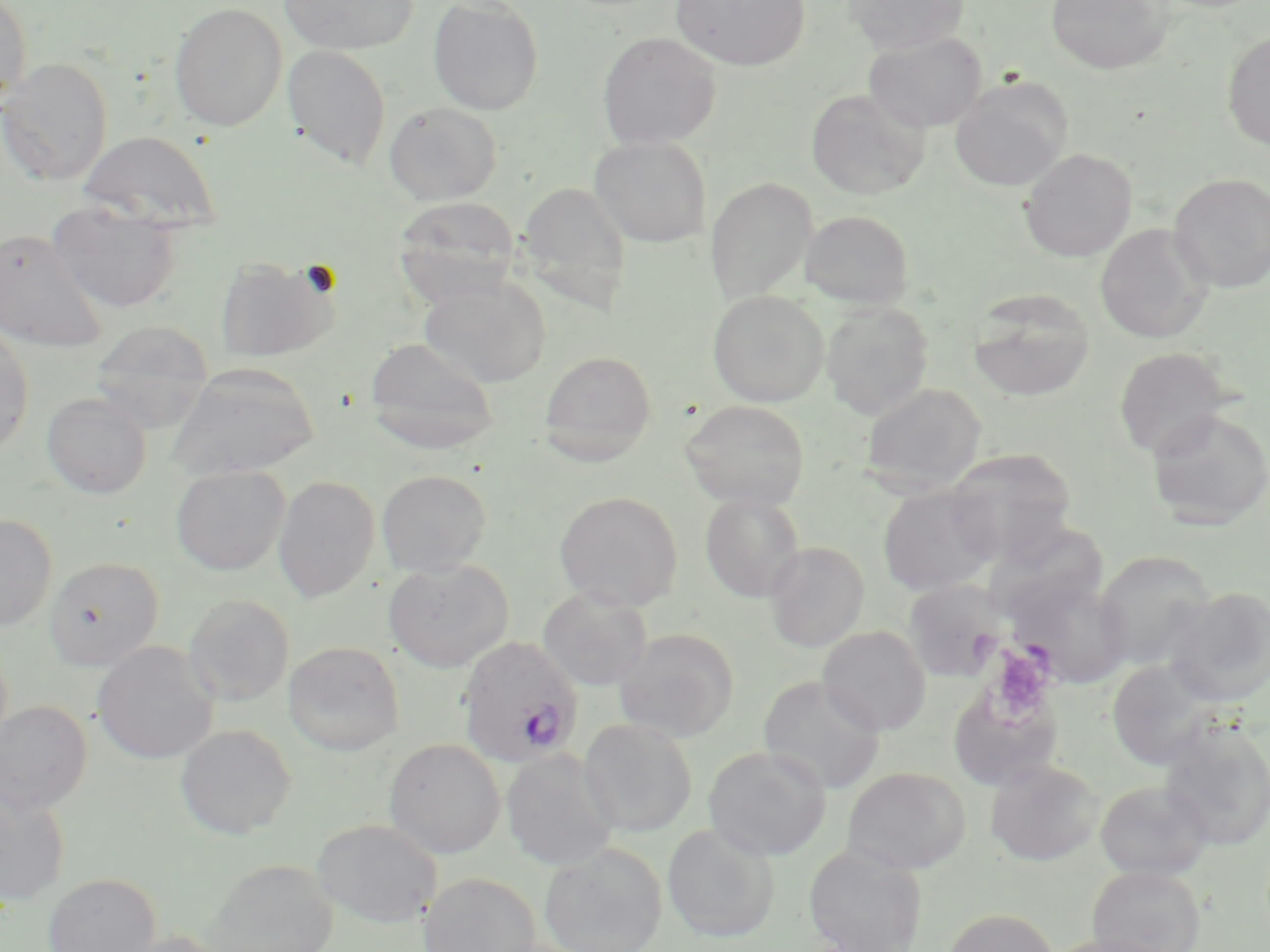 Approximate bounding boxes as (x1, y1, x2, y2) in pixels. Uninfected red blood cell locations: (0, 0, 32, 112), (278, 0, 417, 55), (427, 0, 544, 116), (670, 0, 810, 71), (842, 0, 968, 54), (1046, 0, 1174, 74), (169, 1, 288, 131), (1221, 30, 1270, 151), (597, 31, 722, 150), (863, 31, 987, 132), (281, 44, 392, 168), (0, 57, 113, 185), (949, 75, 1072, 192), (806, 88, 930, 200), (384, 101, 502, 205), (79, 130, 222, 232), (589, 136, 711, 247), (1019, 148, 1137, 261), (1168, 173, 1270, 293), (705, 177, 818, 304), (516, 181, 632, 310), (392, 196, 521, 305), (47, 202, 183, 314), (799, 210, 914, 309), (1095, 223, 1212, 343), (0, 228, 109, 354), (215, 255, 341, 362), (419, 277, 552, 387), (968, 287, 1095, 401), (707, 290, 829, 407), (821, 301, 934, 419), (89, 319, 215, 432), (0, 323, 35, 457), (364, 337, 500, 453), (1112, 347, 1233, 461), (538, 350, 657, 465), (167, 362, 320, 479), (859, 383, 987, 495), (42, 392, 151, 498), (680, 399, 811, 510), (1146, 408, 1270, 530), (944, 447, 1078, 563), (171, 465, 291, 575), (377, 469, 492, 576), (273, 475, 380, 602), (878, 485, 998, 596), (554, 490, 684, 611), (700, 492, 805, 602), (0, 514, 58, 631), (764, 542, 869, 652), (1094, 550, 1216, 670), (44, 557, 164, 669), (383, 559, 514, 671), (1006, 573, 1133, 688), (903, 579, 1008, 682), (537, 587, 653, 691), (1164, 587, 1270, 706), (183, 594, 294, 707), (818, 625, 931, 735), (614, 627, 740, 742), (283, 640, 405, 755), (93, 641, 219, 764), (1107, 660, 1218, 770), (757, 675, 886, 794), (947, 685, 1062, 792), (0, 700, 93, 815), (578, 718, 698, 836), (1158, 720, 1270, 851), (175, 723, 297, 839), (383, 738, 505, 859), (703, 745, 832, 861), (501, 748, 620, 870), (984, 759, 1104, 866), (842, 766, 971, 873), (1094, 780, 1213, 880), (0, 787, 70, 907), (312, 818, 442, 927), (662, 823, 779, 942), (538, 841, 668, 952), (803, 843, 928, 952), (206, 860, 338, 952), (1086, 864, 1206, 952), (43, 873, 161, 952), (418, 873, 542, 952), (942, 908, 1060, 952), (112, 930, 235, 952), (1045, 934, 1177, 952). Plasmodium ovale-infected red blood cell locations: (456, 635, 584, 768). Platelet locations: (988, 646, 1056, 719). Slide-level diagnosis: Plasmodium ovale. Thin blood film. Single field of view. 1000x magnification. May-Grünwald-Giemsa-stained preparation. Light microscopy. Image is 1270×952 pixels.